Report the malaria status of this cell.
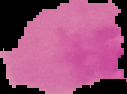
It is uninfected.

preparation = thin blood smear
image size = 127×94 pixels
image type = cell region segmented out of the field of view; surrounding area masked to black